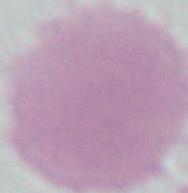
modality = micrograph
magnification = 1000x
identification = erythrocyte